Point out each Plasmodium parasite.
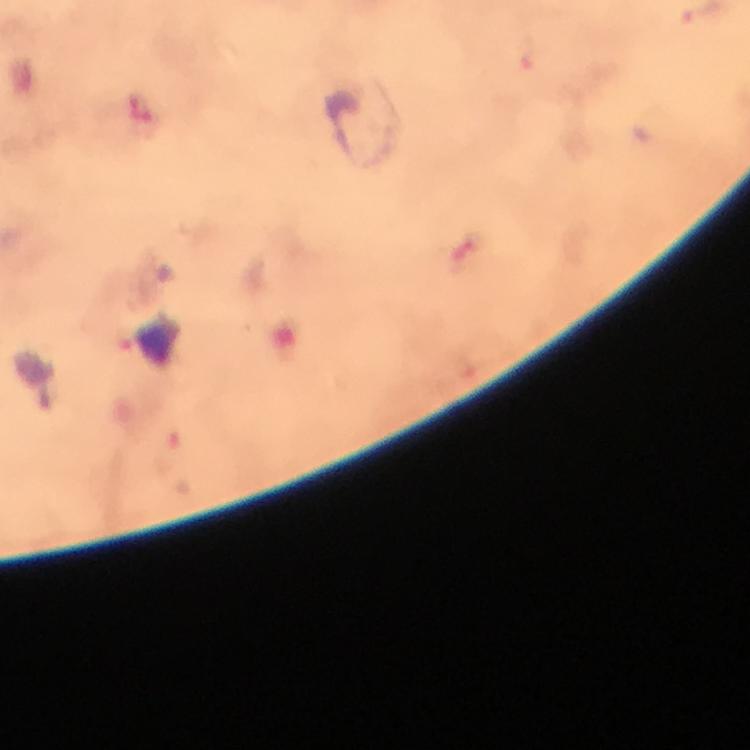
Approximate centers as {x, y} in pixels.
Plasmodium parasites: {523, 57}.

immersion oil = applied
preparation = thick smear
cropped from = a single field of view
stain = Giemsa
capture = smartphone photograph through a microscope
image size = 750×750 pixels
context = from a malaria diagnostic workup
magnification = 100x